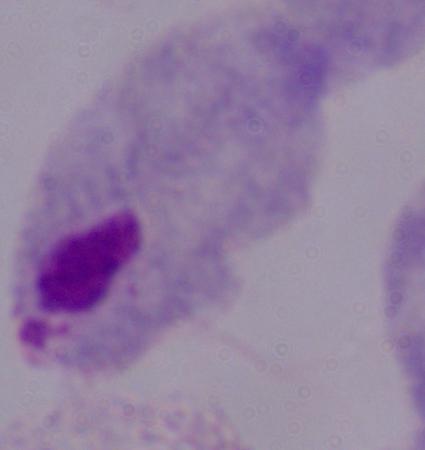 A trichomonad is shown. Captured at 1000x magnification. Photomicrograph.